Classify this cell by malaria status.
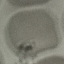

It is uninfected.

image_type: automatically extracted cell patch, resized to 64 × 64 pixels
preparation: thin blood smear
stain: Giemsa
capture: smartphone through the microscope eyepiece